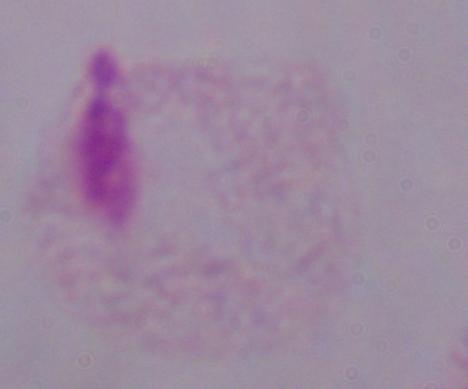
identification: trichomonad
magnification: 1000x
modality: micrograph